Identify the blood parasite species.
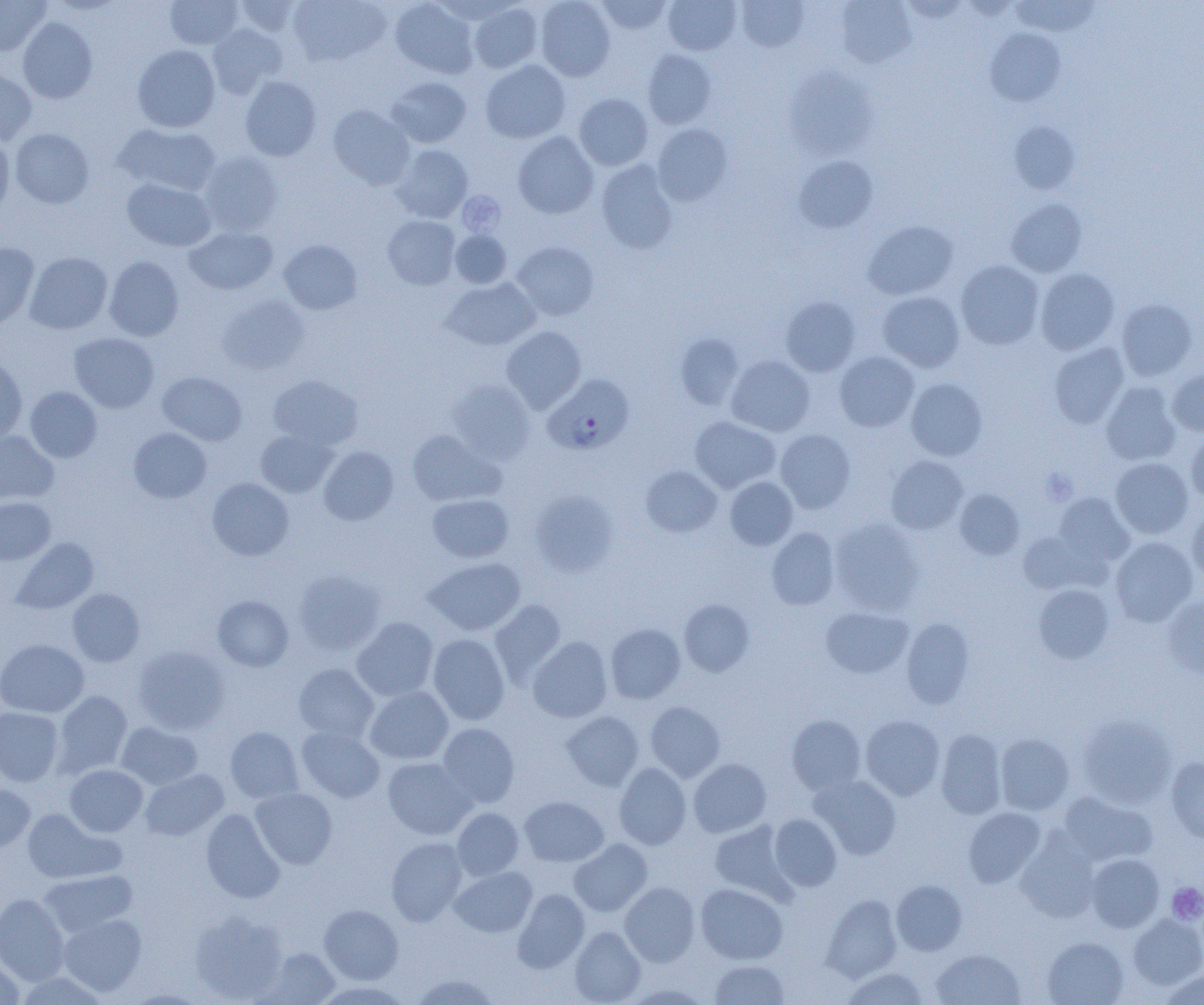
Plasmodium falciparum.

uninfected red blood cell locations = approximate bounding boxes as (x1, y1, x2, y2) in pixels: (0, 0, 51, 55), (165, 0, 243, 50), (231, 0, 303, 38), (288, 0, 391, 67), (390, 0, 479, 78), (535, 0, 616, 82), (595, 0, 673, 35), (663, 0, 741, 55), (736, 0, 808, 53), (1010, 0, 1101, 36), (835, 1, 916, 68), (468, 3, 543, 74), (18, 17, 97, 103), (207, 23, 287, 98), (985, 28, 1066, 106), (132, 45, 220, 132), (642, 50, 716, 128), (480, 60, 570, 143), (784, 67, 878, 160), (0, 70, 36, 145), (240, 76, 321, 161), (385, 76, 471, 148), (574, 93, 653, 170), (328, 105, 415, 189), (1008, 122, 1081, 195), (114, 123, 221, 196), (652, 124, 733, 207), (10, 128, 94, 208), (513, 132, 599, 219), (0, 134, 14, 218), (392, 145, 473, 222), (198, 150, 284, 235), (794, 155, 878, 233), (596, 160, 678, 254), (122, 178, 216, 251), (1006, 198, 1087, 277), (383, 215, 461, 289), (864, 220, 959, 300), (185, 225, 278, 295), (450, 229, 512, 288), (279, 240, 363, 315), (512, 242, 599, 321), (0, 243, 40, 329), (24, 252, 113, 334), (104, 256, 184, 341), (956, 260, 1044, 350), (1035, 268, 1120, 355), (440, 278, 541, 350), (878, 291, 965, 372), (216, 295, 310, 376), (781, 296, 860, 377), (1116, 299, 1197, 381), (501, 326, 586, 413), (69, 332, 159, 413), (674, 333, 745, 410), (1049, 342, 1129, 429), (835, 351, 919, 432), (725, 355, 815, 437), (0, 357, 27, 444), (1167, 367, 1204, 436), (157, 371, 246, 445), (268, 374, 364, 450), (906, 378, 987, 461), (447, 379, 536, 463), (1101, 382, 1181, 465), (25, 386, 102, 462), (689, 416, 780, 493), (129, 427, 212, 504), (255, 429, 338, 497), (407, 429, 504, 506), (775, 429, 856, 513), (1185, 430, 1204, 503), (0, 431, 58, 504), (318, 445, 399, 525), (885, 456, 968, 534), (1110, 457, 1193, 538), (641, 465, 722, 537), (725, 477, 798, 550), (207, 478, 294, 561), (955, 489, 1024, 559), (529, 490, 618, 577), (1054, 492, 1134, 566), (427, 493, 514, 563), (0, 497, 55, 565), (1186, 508, 1204, 586), (829, 519, 925, 614), (766, 527, 839, 610), (1017, 530, 1104, 595), (1110, 536, 1198, 627), (12, 537, 99, 614), (423, 557, 526, 636), (292, 569, 387, 656), (1033, 584, 1114, 663), (67, 588, 145, 667), (212, 594, 294, 672), (1163, 597, 1204, 679), (679, 599, 754, 677), (489, 600, 566, 683), (820, 606, 912, 678), (352, 616, 439, 702), (901, 618, 974, 708), (605, 623, 685, 704), (428, 634, 510, 725), (528, 636, 613, 723), (0, 639, 89, 717), (133, 645, 230, 735), (293, 663, 379, 743), (365, 686, 453, 764), (54, 691, 132, 776), (646, 701, 725, 781), (0, 707, 63, 786), (561, 711, 643, 791), (787, 715, 865, 794), (860, 715, 945, 800), (1078, 715, 1177, 807), (117, 721, 203, 789), (438, 722, 519, 808), (225, 726, 303, 803), (297, 727, 385, 803), (936, 727, 1006, 819), (995, 734, 1074, 815), (382, 756, 476, 840), (1166, 757, 1204, 843), (688, 758, 771, 837), (614, 762, 691, 849), (65, 764, 148, 837), (139, 769, 228, 841), (810, 775, 901, 859), (0, 783, 35, 855), (250, 787, 338, 869), (1059, 792, 1157, 867), (519, 796, 609, 867), (452, 807, 524, 880), (963, 807, 1046, 888), (22, 808, 123, 884), (201, 808, 285, 903), (769, 814, 842, 891), (709, 821, 791, 899), (1017, 830, 1100, 922), (385, 837, 468, 925), (569, 839, 652, 917), (1086, 854, 1164, 932), (449, 865, 536, 937), (38, 869, 138, 937), (891, 879, 967, 956), (620, 881, 700, 967), (695, 883, 787, 964), (513, 888, 590, 972), (0, 893, 69, 985), (822, 894, 902, 982), (319, 904, 403, 984), (189, 910, 288, 1003), (58, 914, 147, 997), (1129, 914, 1204, 989), (569, 926, 646, 1005), (1042, 937, 1128, 1005), (257, 947, 340, 1005), (931, 949, 1025, 1005), (0, 956, 24, 1005), (709, 960, 789, 1004), (841, 967, 930, 1004), (1160, 969, 1204, 1005), (15, 972, 110, 1005), (409, 973, 501, 1005)
platelet locations = approximate bounding boxes as (x1, y1, x2, y2) in pixels: (457, 191, 505, 236), (1040, 468, 1078, 505), (1167, 882, 1204, 924)
image size = 1204×1005 pixels
Plasmodium falciparum-infected red blood cell locations = approximate bounding boxes as (x1, y1, x2, y2) in pixels: (544, 375, 633, 455)
field of view = one of a larger specimen
modality = optical microscopy
magnification = 1000x
preparation = thin blood smear